Give the extent of all Plasmodium malariae-infected red blood cells.
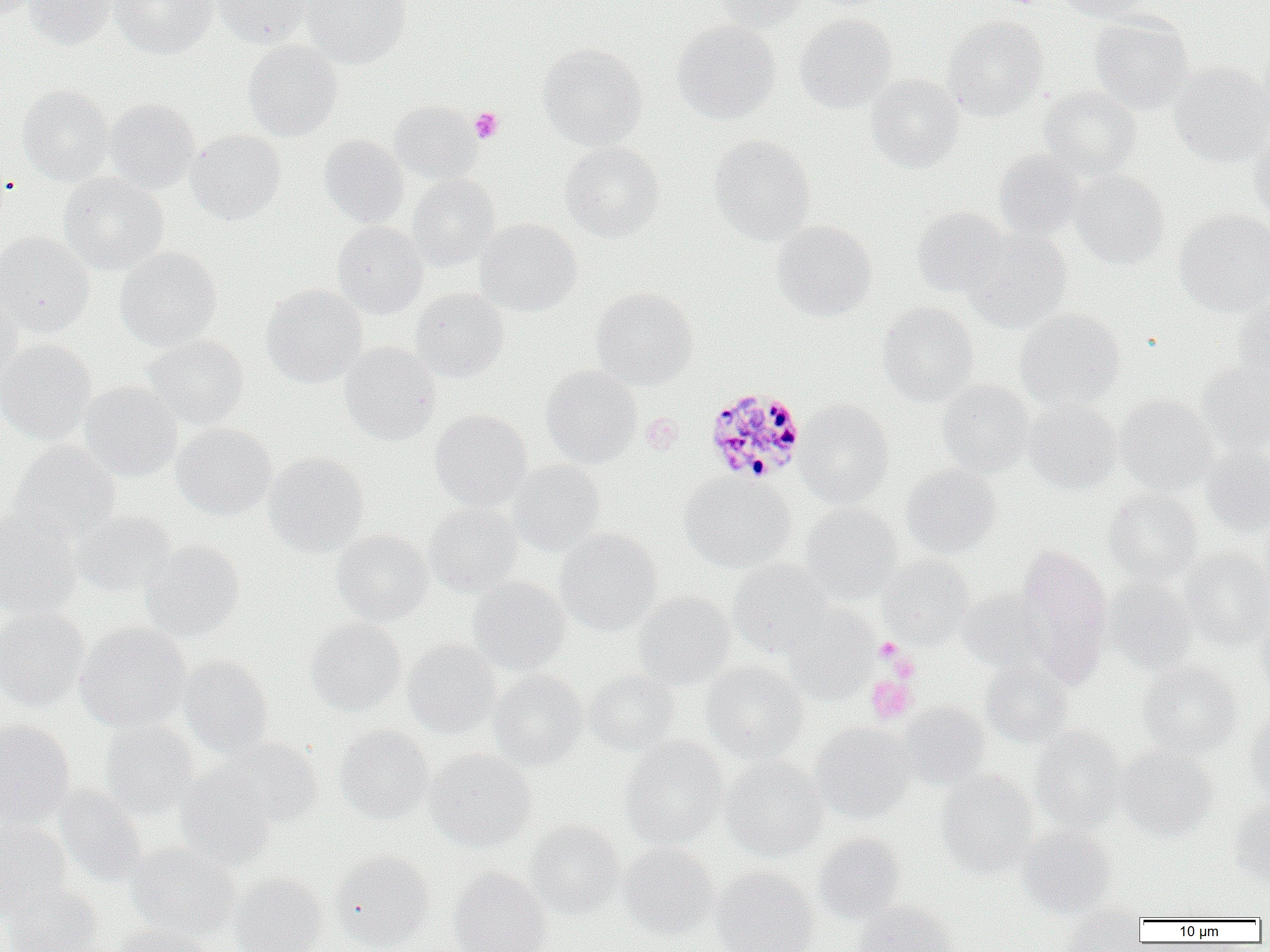
Approximate bounding boxes as (x1,y1)-(x2,y2) corner pairs in pixels.
Plasmodium malariae-infected red blood cells: (703,388)-(808,485).

Uninfected red blood cell locations: (0,0)-(42,18), (22,0)-(115,49), (110,0)-(217,59), (213,0)-(315,47), (302,0)-(412,69), (711,0)-(809,30), (1056,0)-(1157,21), (1090,13)-(1193,115), (795,14)-(897,112), (944,16)-(1048,119), (672,19)-(780,124), (243,40)-(342,142), (538,44)-(647,150), (1169,62)-(1270,166), (866,74)-(963,172), (17,85)-(113,185), (1040,85)-(1142,179), (105,98)-(199,193), (390,101)-(481,184), (186,129)-(286,224), (1248,131)-(1270,222), (320,134)-(409,227), (710,135)-(815,244), (561,141)-(664,242), (993,150)-(1084,240), (1070,169)-(1169,269), (58,172)-(168,275), (407,174)-(500,271), (913,207)-(1011,299), (1174,210)-(1270,317), (475,218)-(581,316), (332,221)-(427,318), (772,221)-(877,320), (964,228)-(1072,333), (0,231)-(95,336), (115,247)-(221,350), (261,284)-(367,388), (411,287)-(508,381), (591,287)-(698,388), (0,288)-(23,395), (1233,299)-(1270,393), (877,302)-(978,407), (1015,309)-(1125,410), (142,334)-(249,430), (0,339)-(96,444), (340,342)-(441,445), (1195,363)-(1270,455), (542,366)-(641,468), (937,379)-(1034,477), (81,381)-(182,481), (1116,395)-(1218,495), (1023,399)-(1121,493), (794,401)-(893,508), (430,410)-(532,511), (171,423)-(276,520), (10,442)-(121,544), (1201,444)-(1270,538), (264,452)-(368,556), (507,459)-(605,554), (901,464)-(1001,558), (680,473)-(794,572), (1104,488)-(1203,585), (424,503)-(523,596), (800,503)-(902,603), (0,509)-(83,619), (70,510)-(177,598), (1258,515)-(1270,609), (556,528)-(661,636), (332,530)-(433,625), (142,540)-(244,641), (1014,548)-(1113,680), (1179,548)-(1270,649), (878,554)-(974,647), (728,559)-(832,658), (1103,577)-(1197,674), (467,578)-(570,673), (956,589)-(1050,671), (634,591)-(736,689), (783,605)-(878,701), (0,607)-(89,711), (1254,614)-(1270,702), (306,617)-(406,716), (75,622)-(191,732), (402,639)-(501,737), (178,654)-(273,757), (981,659)-(1073,747), (1138,661)-(1243,759), (701,662)-(807,763), (488,670)-(586,769), (585,670)-(679,755), (898,703)-(990,790), (1245,711)-(1270,807), (99,719)-(200,818), (0,720)-(75,828), (810,723)-(915,822), (334,724)-(434,823), (1030,727)-(1128,831), (214,737)-(323,828), (621,738)-(728,848), (1118,745)-(1216,841), (426,748)-(537,851), (721,756)-(828,860), (174,767)-(277,870), (937,771)-(1038,877), (53,785)-(148,889), (1230,798)-(1270,886), (0,819)-(72,917), (525,820)-(624,919), (1018,827)-(1117,919), (814,833)-(905,924), (620,842)-(719,940), (126,843)-(240,939), (331,851)-(436,951), (712,867)-(818,952), (448,868)-(551,952), (230,873)-(328,952), (2,882)-(104,952), (851,902)-(958,952), (1061,906)-(1147,951), (116,923)-(215,952). Platelet locations: (1002,0)-(1045,9), (469,107)-(504,143), (641,413)-(683,454), (875,637)-(901,663), (890,650)-(919,682), (865,675)-(915,724). Slide-level diagnosis: Plasmodium malariae. One field of a larger specimen. Image is 1270×952 pixels. Light microscopy. Thin blood smear. 1000x magnification.